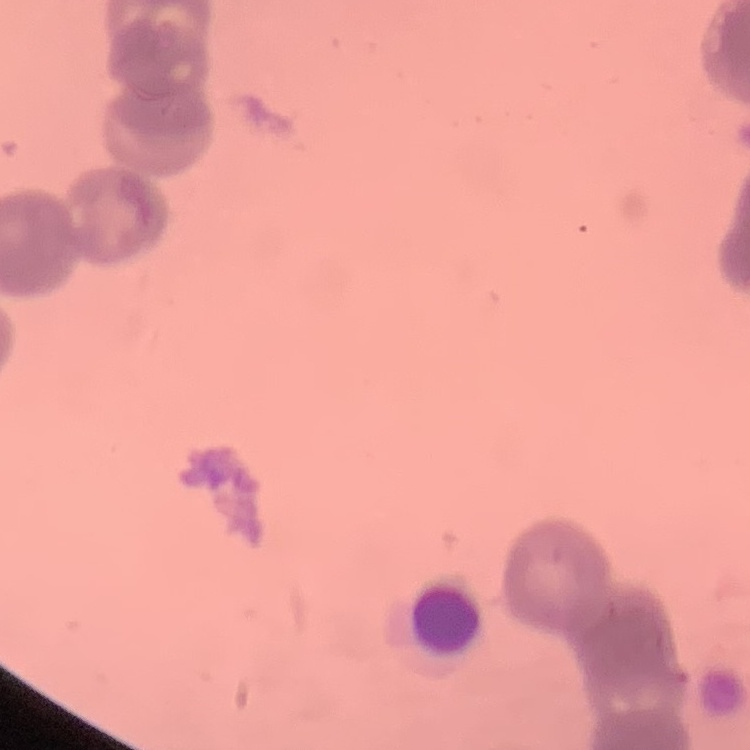 The erythrocytes exhibit rouleaux formation. Thin blood film. One tile cut from a larger photomicrograph. Field's or Giemsa stain.